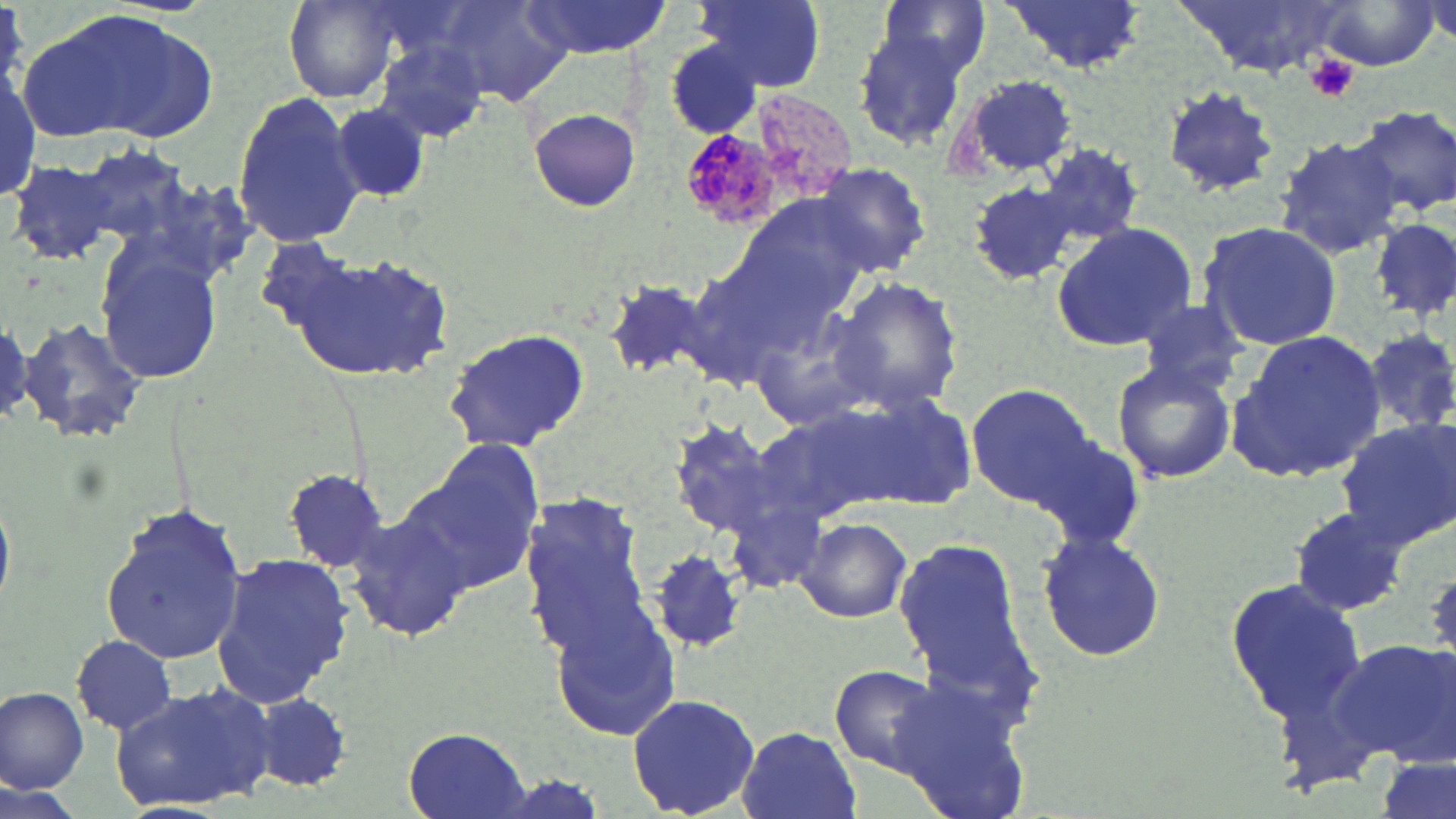

Summary:
  - Coordinate format: approximate bounding boxes as (x1, y1, x2, y2) in pixels
  - Uninfected red blood cell locations: (283, 0, 399, 103), (520, 0, 670, 57), (693, 0, 829, 92), (878, 0, 994, 78), (999, 0, 1144, 73), (1171, 0, 1356, 77), (437, 1, 572, 107), (1311, 1, 1440, 70), (31, 7, 221, 145), (847, 27, 973, 154), (374, 37, 489, 146), (663, 38, 770, 141), (1, 59, 38, 209), (953, 73, 1082, 180), (1161, 84, 1278, 198), (232, 93, 367, 250), (331, 104, 432, 203), (1351, 105, 1456, 215), (528, 108, 642, 212), (1273, 133, 1404, 261), (76, 144, 190, 255), (1039, 144, 1144, 244), (8, 158, 118, 266), (810, 159, 932, 276), (965, 181, 1078, 286), (737, 193, 875, 321), (1373, 220, 1454, 317), (1052, 222, 1197, 353), (1197, 222, 1342, 352), (272, 243, 460, 386), (93, 245, 225, 387), (675, 259, 808, 395), (827, 275, 966, 418), (603, 277, 721, 384), (1135, 301, 1250, 397), (746, 306, 882, 436), (19, 317, 148, 444), (442, 328, 593, 455), (1228, 330, 1387, 480), (1112, 358, 1237, 485), (964, 381, 1095, 506), (832, 390, 978, 511), (746, 408, 898, 530), (1337, 417, 1456, 547), (663, 419, 799, 544), (1032, 432, 1146, 552), (410, 446, 544, 593), (283, 466, 393, 573), (0, 482, 15, 611), (723, 485, 829, 597), (518, 495, 655, 655), (100, 505, 247, 667), (1287, 505, 1412, 619), (346, 506, 470, 644), (791, 514, 914, 624), (1034, 530, 1168, 660), (894, 534, 1037, 697), (649, 550, 745, 654), (211, 552, 351, 708), (1225, 577, 1368, 724), (548, 598, 686, 746), (70, 634, 177, 735), (1337, 641, 1456, 767), (828, 663, 947, 775), (882, 670, 1034, 819), (112, 682, 276, 814), (0, 686, 89, 794), (247, 691, 352, 793), (627, 693, 762, 818), (736, 726, 862, 819), (404, 728, 530, 819), (1376, 754, 1455, 819)
  - Plasmodium malariae-infected red blood cell locations: (748, 89, 857, 201), (682, 129, 776, 229)
  - Platelet locations: (1304, 53, 1360, 103)
  - Slide-level diagnosis: Plasmodium malariae
  - Modality: optical microscopy
  - Image size: 1456×819 pixels
  - Magnification: 1000x
  - Field of view: one of a larger specimen
  - Preparation: thin blood film
  - Stain: May-Grünwald-Giemsa